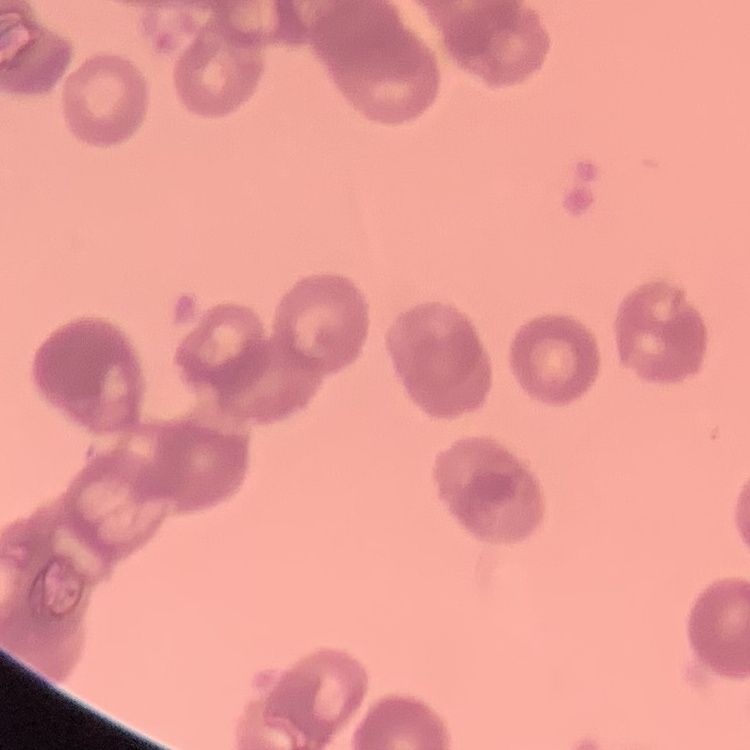 The red blood cells show rouleaux formation. Square crop of a larger photomicrograph. Stained with either Field's or Giemsa. Thin blood smear.